Give the position of every leukocyte visible.
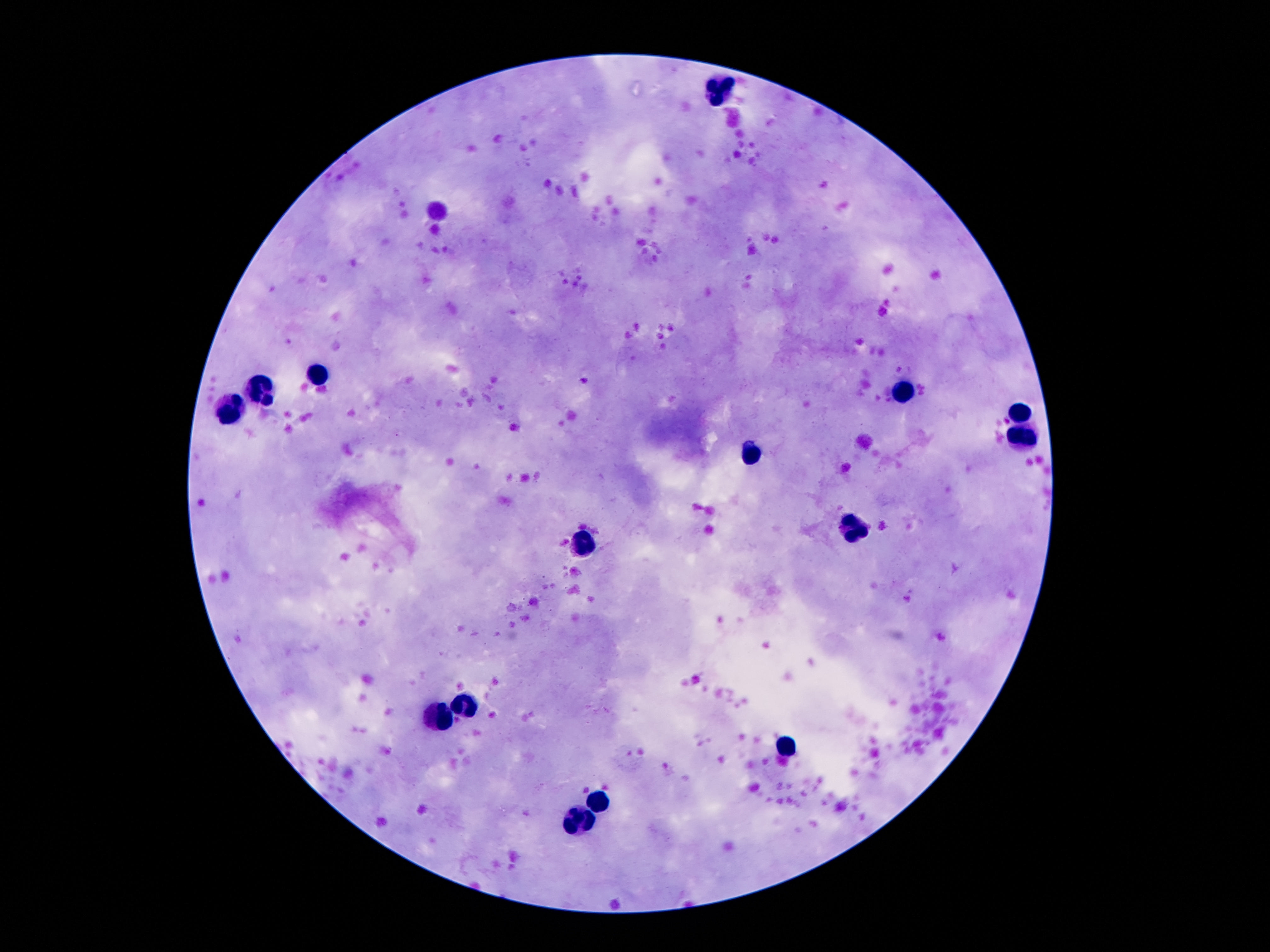

Approximate centers as (x, y) in pixels.
Leukocytes: (722, 92), (317, 374), (901, 389), (264, 395), (233, 410), (1018, 414), (1022, 435), (756, 452), (848, 530), (583, 544), (468, 701), (434, 716), (787, 745), (598, 798), (575, 822).

field of view = one from this slide
patient malaria status = negative
capture = smartphone camera through the microscope eyepiece
magnification = 100x
image size = 1270×952 pixels
preparation = thick blood film
stain = Giemsa